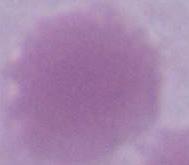
Micrograph. An erythrocyte is shown. Captured at 1000x magnification.